Report the malaria status of this cell.
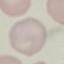
Uninfected.

Summary:
  - Stain: Giemsa
  - Preparation: thin blood smear
  - Image type: automatically extracted cell patch, resized to 64 × 64 pixels
  - Capture: smartphone camera at the microscope eyepiece